Name the blood parasite species.
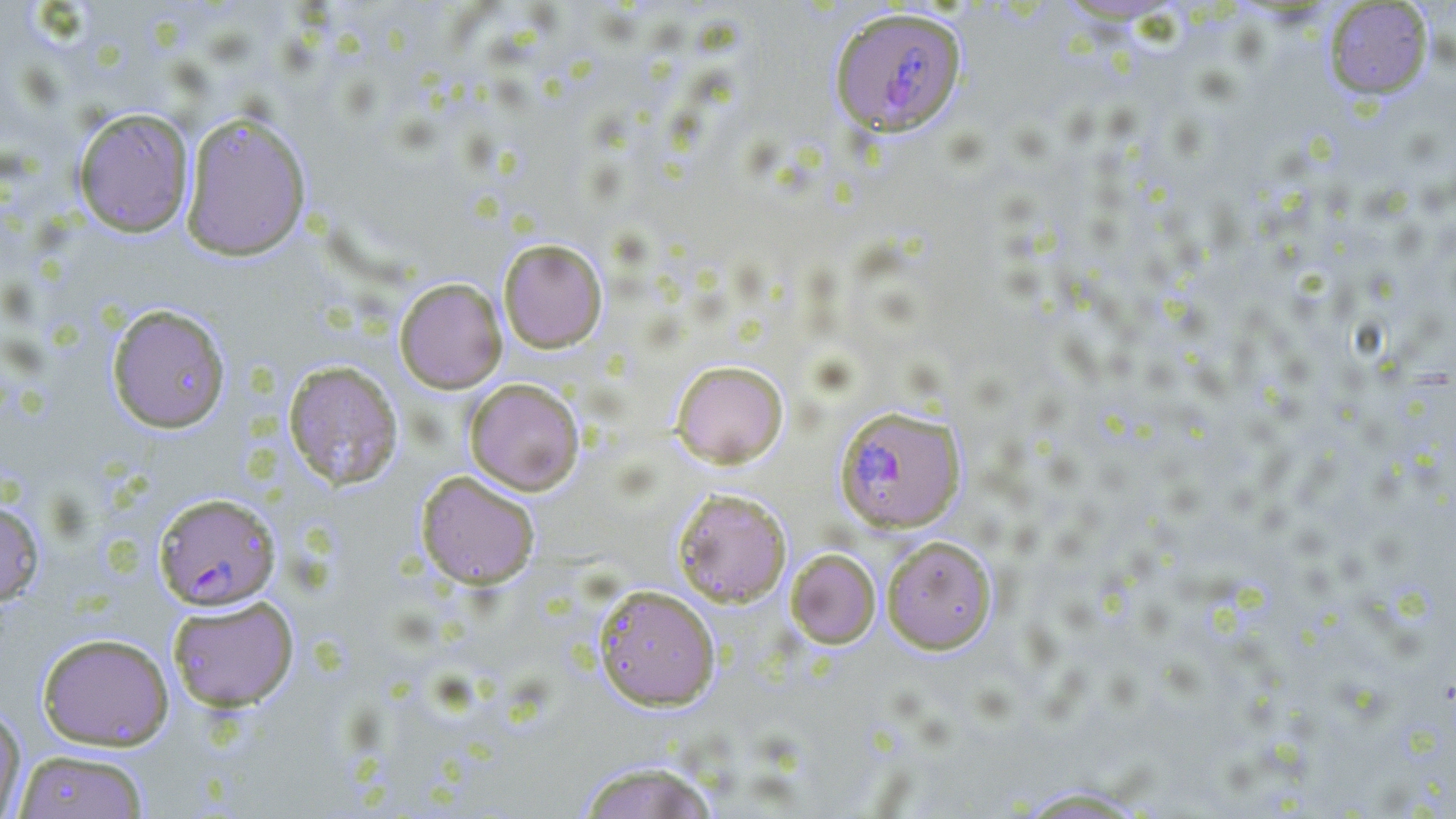
Plasmodium falciparum.

Approximate bounding boxes as (x1, y1, x2, y2) in pixels. Uninfected red blood cell locations: (1323, 1, 1434, 101), (73, 107, 194, 237), (180, 111, 312, 261), (497, 238, 608, 353), (394, 277, 507, 394), (106, 304, 231, 434), (282, 360, 403, 490), (670, 360, 789, 468), (464, 378, 585, 496), (415, 470, 540, 589), (673, 488, 791, 606), (0, 499, 44, 607), (881, 535, 997, 654), (785, 548, 881, 648), (593, 584, 720, 711), (167, 595, 299, 711), (36, 632, 174, 751), (0, 701, 26, 818), (12, 749, 151, 818), (575, 761, 719, 819), (1011, 786, 1156, 818). Plasmodium falciparum-infected red blood cell locations: (829, 7, 967, 139), (834, 404, 965, 533), (154, 491, 281, 610). 1000x magnification. Image is 1456×819 pixels. May-Grünwald-Giemsa stain. Thin blood film. Optical microscopy. One field of a larger specimen.